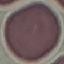
Result: no malaria parasites detected. Giemsa-stained preparation. Thin smear of blood. Automatically extracted cell patch, resized to 64 × 64 pixels. Acquired by smartphone through the microscope eyepiece.